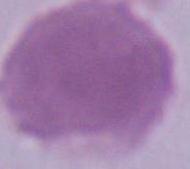
Summary:
  - Identification: red blood cell
  - Modality: micrograph
  - Magnification: 1000x